Classify the preparation.
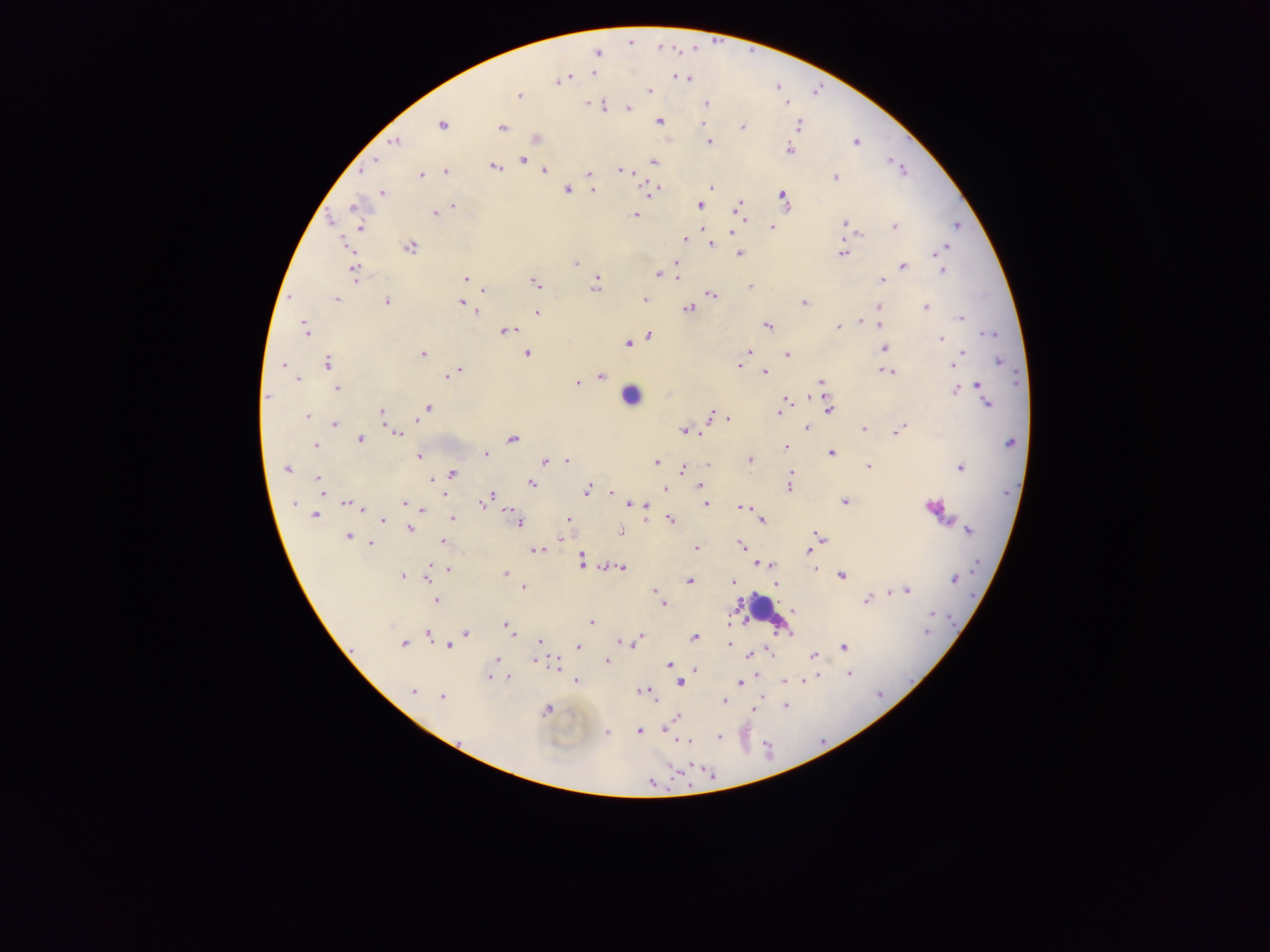
Thick blood smear.

Approximate centers as x y in pixels.
Summary:
  - Plasmodium parasite locations: 598 52; 594 73; 678 77; 686 79; 560 81; 650 91; 518 96; 786 101; 588 103; 706 103; 603 105; 629 107; 659 122; 704 124; 799 124; 442 126; 741 127; 502 128; 395 141; 709 142; 856 142; 790 149; 376 160; 523 161; 654 162; 493 167; 363 170; 544 171; 621 171; 446 172; 589 173; 421 175; 835 177; 711 186; 567 189; 592 190; 382 193; 651 193; 783 195; 453 205; 700 205; 355 207; 738 207; 434 213; 741 215; 635 216; 845 223; 894 226; 957 226; 772 227; 361 228; 731 232; 857 232; 686 239; 345 243; 711 245; 409 247; 947 248; 935 253; 740 254; 841 254; 576 262; 676 262; 903 266; 941 270; 355 272; 658 274; 886 274; 676 278; 465 279; 882 280; 536 284; 595 285; 749 287; 483 290; 712 295; 879 299; 337 300; 645 300; 386 302; 462 303; 804 303; 925 307; 688 308; 879 308; 476 312; 537 313; 960 318; 860 320; 767 325; 879 325; 837 327; 305 330; 508 330; 990 334; 649 336; 941 339; 632 342; 628 344; 885 347; 749 351; 963 352; 527 353; 423 354; 787 355; 957 360; 999 360; 328 364; 282 365; 739 365; 952 365; 459 371; 764 372; 888 372; 449 375; 601 376; 298 379; 821 382; 577 383; 979 385; 337 389; 956 391; 266 397; 786 400; 986 402; 427 407; 829 410; 381 411; 779 413; 307 416; 712 416; 728 419; 335 425; 806 428; 863 429; 899 429; 684 431; 701 433; 397 434; 512 438; 359 439; 1011 443; 316 446; 787 447; 831 453; 486 454; 418 457; 544 460; 750 460; 567 461; 657 461; 708 465; 869 466; 960 467; 287 468; 683 470; 452 474; 791 474; 439 477; 318 479; 432 479; 790 480; 531 484; 700 486; 666 488; 789 488; 587 491; 320 492; 611 492; 446 494; 491 495; 404 502; 844 502; 294 504; 482 504; 628 504; 641 504; 706 504; 348 505; 645 507; 741 507; 360 508; 423 510; 510 513; 315 515; 453 518; 568 519; 671 520; 384 521; 761 521; 518 522; 410 529; 968 530; 621 532; 348 537; 819 537; 560 539; 443 542; 371 544; 741 545; 697 547; 538 551; 809 551; 582 558; 760 563; 772 566; 620 567; 449 570; 815 570; 504 573; 842 575; 402 576; 427 578; 954 580; 689 581; 733 582; 776 584; 523 588; 656 591; 908 591; 866 600; 436 601; 663 604; 793 611; 932 614; 591 623; 391 625; 505 625; 927 632; 465 633; 511 634; 427 635; 695 636; 640 637; 540 641; 636 641; 620 642; 629 643; 729 644; 403 645; 449 646; 579 648; 844 648; 815 655; 751 656; 497 660; 534 661; 606 662; 554 664; 669 664; 848 674; 509 677; 488 678; 813 678; 576 681; 785 681; 805 681; 680 683; 740 683; 413 691; 645 693; 762 696; 442 697; 724 700; 786 706; 754 710; 546 711; 677 717; 639 730; 666 730; 607 733; 719 737; 685 741; 652 783
  - Leukocyte locations: 630 396; 764 610
  - Capture: mobile-phone photograph through a microscope
  - Country: Ghana
  - Field of view: single
  - Image size: 1270×952 pixels